Assess the morphology of the erythrocytes.
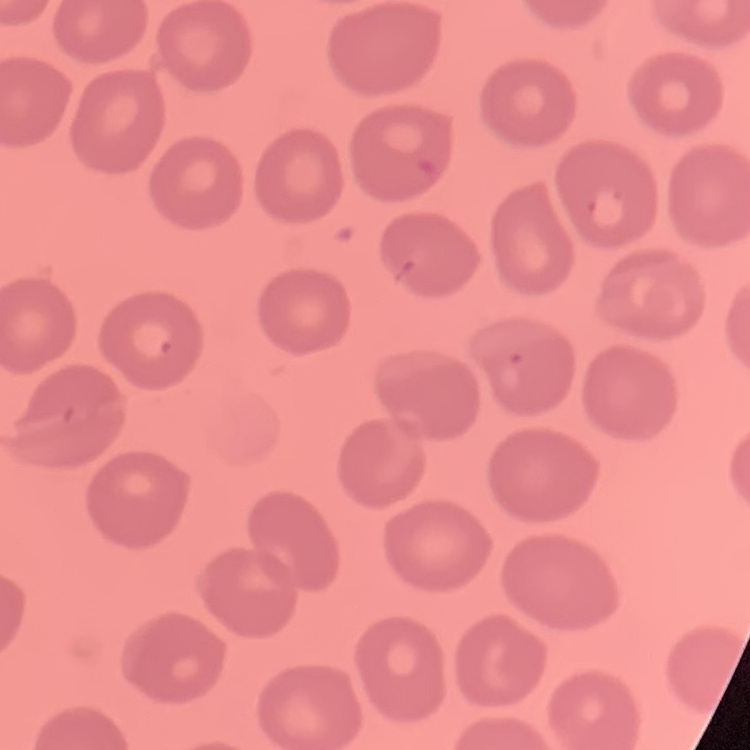
They show no rouleaux formation.

Stained with either Field's or Giemsa. Thin peripheral smear. One tile cut from a larger photomicrograph.